Give the extent of all uninfected red blood cells.
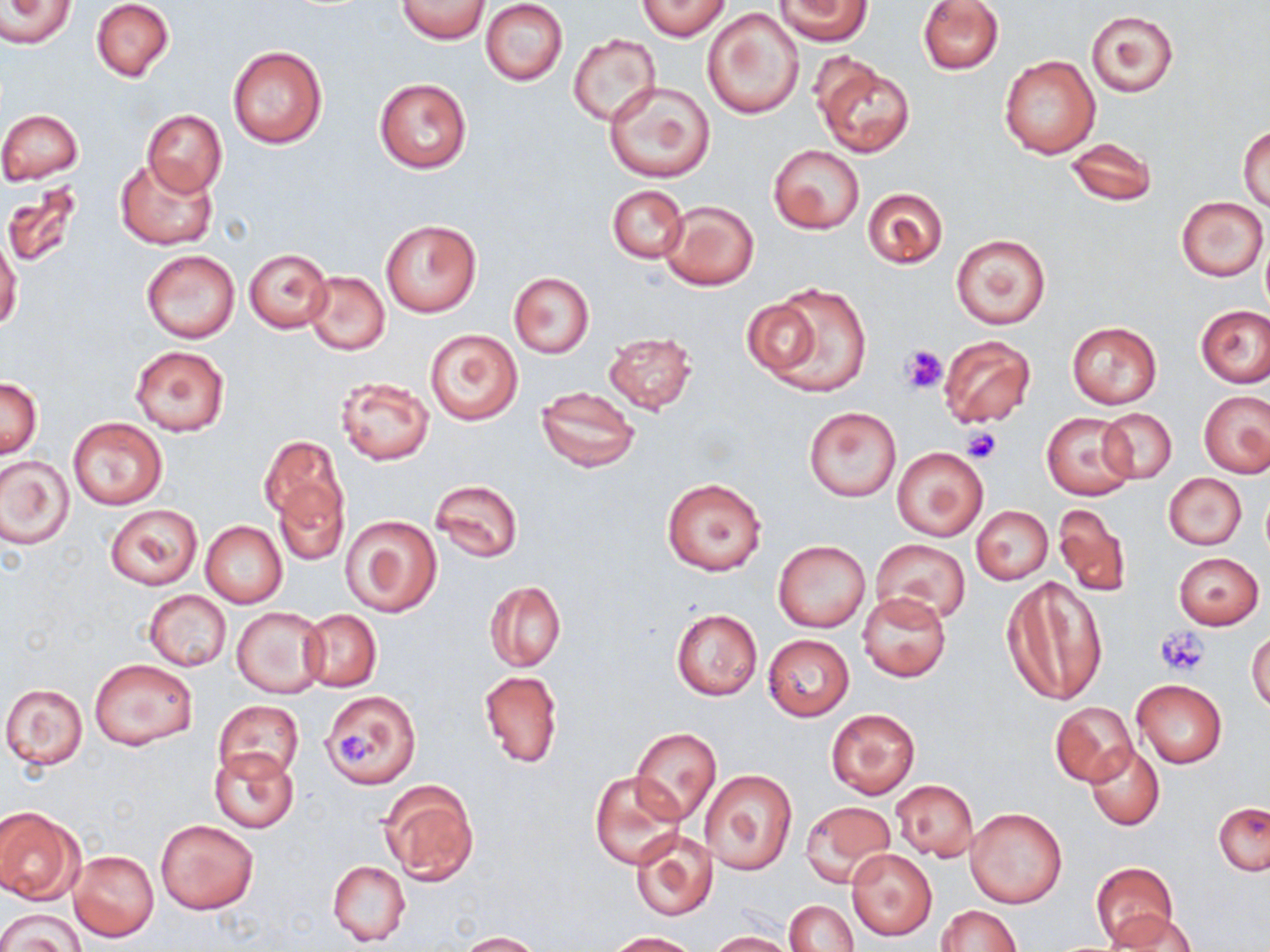
Approximate bounding boxes as (x1, y1, x2, y2) in pixels.
Uninfected red blood cells: (2, 0, 74, 48), (90, 0, 174, 82), (396, 0, 489, 43), (638, 0, 731, 40), (772, 0, 872, 45), (917, 0, 1003, 74), (480, 1, 568, 85), (704, 7, 804, 120), (1085, 9, 1179, 97), (568, 34, 661, 126), (228, 45, 328, 151), (999, 54, 1101, 159), (813, 55, 916, 159), (374, 79, 471, 172), (604, 82, 716, 183), (0, 109, 82, 184), (141, 110, 227, 197), (1239, 125, 1270, 210), (1067, 138, 1157, 207), (770, 145, 865, 234), (115, 158, 219, 248), (2, 183, 86, 271), (606, 185, 688, 262), (861, 187, 949, 270), (1177, 197, 1268, 280), (660, 199, 759, 291), (381, 219, 482, 317), (950, 233, 1051, 330), (0, 234, 22, 333), (1260, 237, 1270, 314), (243, 248, 332, 332), (140, 249, 240, 344), (302, 271, 390, 357), (509, 273, 594, 357), (756, 283, 874, 397), (742, 297, 828, 378), (1196, 305, 1269, 387), (1067, 322, 1161, 409), (425, 328, 522, 424), (602, 331, 698, 415), (938, 335, 1037, 428), (129, 344, 229, 436), (334, 375, 436, 466), (0, 377, 42, 458), (535, 386, 641, 473), (1199, 390, 1270, 478), (803, 406, 901, 501), (1099, 409, 1176, 484), (1043, 413, 1137, 500), (67, 417, 168, 509), (260, 435, 345, 525), (893, 447, 987, 541), (0, 454, 74, 549), (1164, 473, 1247, 550), (662, 478, 767, 577), (429, 479, 522, 564), (273, 482, 349, 566), (1052, 502, 1132, 597), (105, 504, 202, 590), (973, 506, 1052, 584), (342, 515, 442, 617), (201, 521, 287, 608), (870, 538, 971, 624), (774, 540, 870, 632), (1174, 552, 1264, 629), (1003, 575, 1107, 707), (484, 580, 565, 672), (144, 590, 232, 672), (858, 591, 950, 681), (231, 607, 327, 697), (671, 608, 762, 700), (301, 609, 381, 691), (1247, 629, 1270, 715), (763, 634, 854, 720), (92, 658, 198, 751), (479, 669, 564, 768), (1132, 679, 1227, 768), (2, 684, 89, 769), (320, 689, 422, 788), (212, 699, 304, 784), (1051, 701, 1138, 787), (827, 707, 921, 799), (631, 727, 721, 826), (1085, 744, 1164, 831), (659, 748, 762, 864), (210, 749, 297, 832), (700, 769, 797, 874), (590, 770, 683, 870), (378, 779, 479, 884), (890, 780, 977, 862), (801, 802, 895, 887), (1213, 802, 1270, 876), (0, 807, 84, 904), (965, 807, 1067, 909), (156, 818, 259, 915), (629, 827, 720, 921), (846, 848, 937, 941), (70, 850, 158, 941), (328, 860, 411, 946), (1089, 862, 1178, 949), (784, 900, 858, 952), (934, 905, 1021, 951), (0, 907, 83, 952), (1109, 911, 1196, 952), (458, 931, 543, 951), (610, 931, 701, 952), (708, 931, 796, 952).

Platelet locations: (901, 345, 946, 394), (961, 427, 1002, 464), (1155, 627, 1210, 676), (336, 733, 380, 769). Slide-level diagnosis: negative for blood parasites. Thin blood film. 1000x magnification. May-Grünwald-Giemsa-stained preparation. Light microscopy. Image is 1270×952 pixels. One field of a larger specimen.